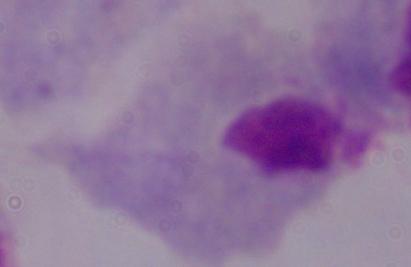
Photomicrograph. 1000x magnification. A trichomonad is shown.